Point out each malaria parasite and each leukocyte.
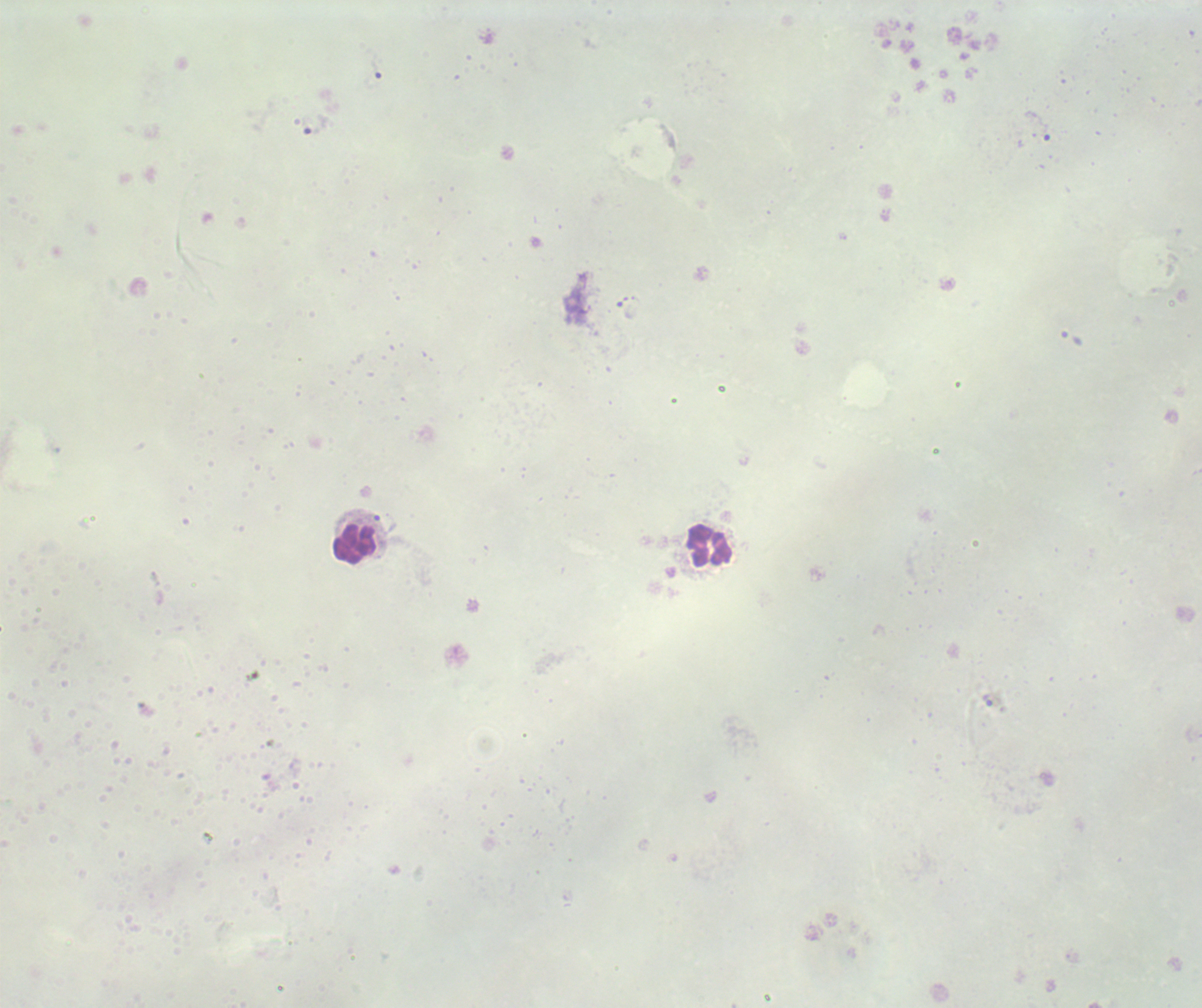

No malaria parasites seen.
Approximate centers as {x, y} in pixels.
Leukocytes: {354, 544}, {710, 544}.

context: previously used in an actual diagnosis
stain: Romanowsky
magnification: 100x
preparation: thick blood smear
field_of_view: single
background_quality: poor
coloration_quality: bad
image_size: 1202×1008 pixels